State which parasite is depicted.
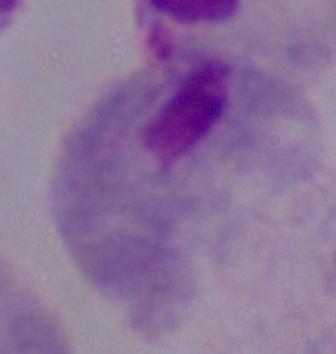

This is a trichomonad.

modality = micrograph
magnification = 1000x